Give the extent of all Plasmodium falciparum-infected red blood cells.
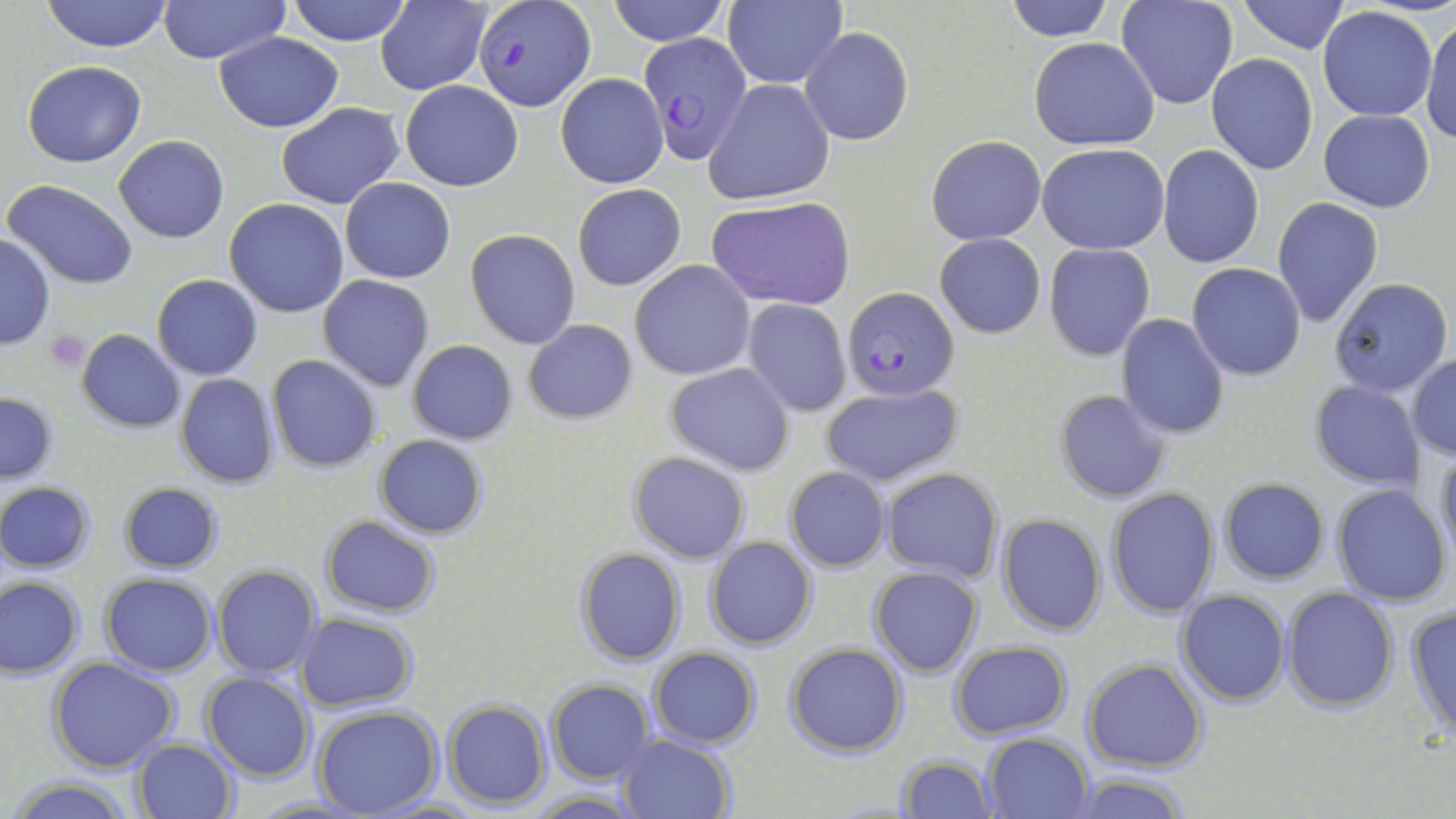
Approximate bounding boxes as (x1,y1)-(x2,y2) corner pairs in pixels.
Plasmodium falciparum-infected red blood cells: (474,1)-(595,111), (641,33)-(752,165), (842,287)-(960,400).

Summary:
  - Platelet locations: (45,330)-(91,372)
  - Uninfected red blood cell locations: (40,0)-(173,52), (158,0)-(292,66), (284,0)-(414,45), (604,0)-(731,46), (1006,0)-(1114,42), (1237,0)-(1350,54), (723,1)-(847,88), (1115,1)-(1237,111), (376,2)-(490,95), (1318,7)-(1437,121), (1421,14)-(1456,147), (800,26)-(913,145), (214,32)-(344,131), (1030,38)-(1159,150), (1206,54)-(1317,175), (22,61)-(147,166), (554,72)-(668,189), (704,79)-(834,205), (400,81)-(525,191), (275,102)-(405,209), (1319,110)-(1436,212), (114,135)-(228,242), (927,135)-(1046,244), (1038,143)-(1168,254), (1157,146)-(1264,267), (340,177)-(456,283), (4,180)-(139,290), (572,183)-(686,290), (223,198)-(349,318), (706,198)-(854,312), (1273,198)-(1383,327), (465,228)-(581,349), (935,233)-(1046,339), (0,235)-(54,350), (1044,243)-(1154,360), (630,259)-(755,381), (1186,263)-(1307,381), (152,275)-(263,380), (318,275)-(433,391), (1329,277)-(1453,396), (743,299)-(852,418), (1116,314)-(1230,440), (521,320)-(638,423), (76,330)-(185,432), (407,339)-(518,445), (267,355)-(380,472), (1407,355)-(1456,460), (664,362)-(794,476), (175,373)-(280,489), (1308,381)-(1426,491), (819,383)-(964,488), (1053,389)-(1170,502), (0,391)-(59,484), (373,434)-(490,539), (1436,444)-(1456,563), (627,451)-(751,564), (784,467)-(892,572), (880,469)-(1003,582), (1219,479)-(1328,584), (1,481)-(96,572), (117,481)-(226,573), (1331,484)-(1452,607), (1105,487)-(1219,618), (996,514)-(1107,637), (320,516)-(443,618), (705,537)-(817,651), (574,548)-(685,665), (212,565)-(322,678), (868,566)-(984,677), (99,572)-(218,674), (0,576)-(85,678), (1282,587)-(1399,711), (1176,590)-(1290,706), (1405,604)-(1456,738), (295,612)-(418,710), (948,641)-(1073,740), (784,642)-(909,756), (648,647)-(761,747), (48,658)-(181,773), (1082,658)-(1208,772), (202,672)-(315,781), (547,680)-(655,784), (443,700)-(550,808), (313,707)-(441,818), (982,732)-(1092,817), (616,733)-(734,818), (134,738)-(238,819), (895,754)-(997,819), (1065,774)-(1192,818), (9,775)-(134,818), (527,790)-(650,818), (366,796)-(489,817), (251,797)-(369,818)
  - Slide-level diagnosis: Plasmodium falciparum
  - Modality: optical microscopy
  - Image size: 1456×819 pixels
  - Magnification: 1000x
  - Stain: May-Grünwald-Giemsa
  - Preparation: thin blood smear
  - Field of view: single